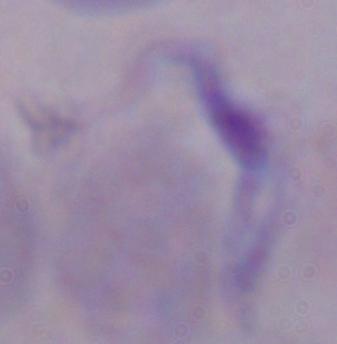

1000x magnification. Photomicrograph. A trypanosome is seen.